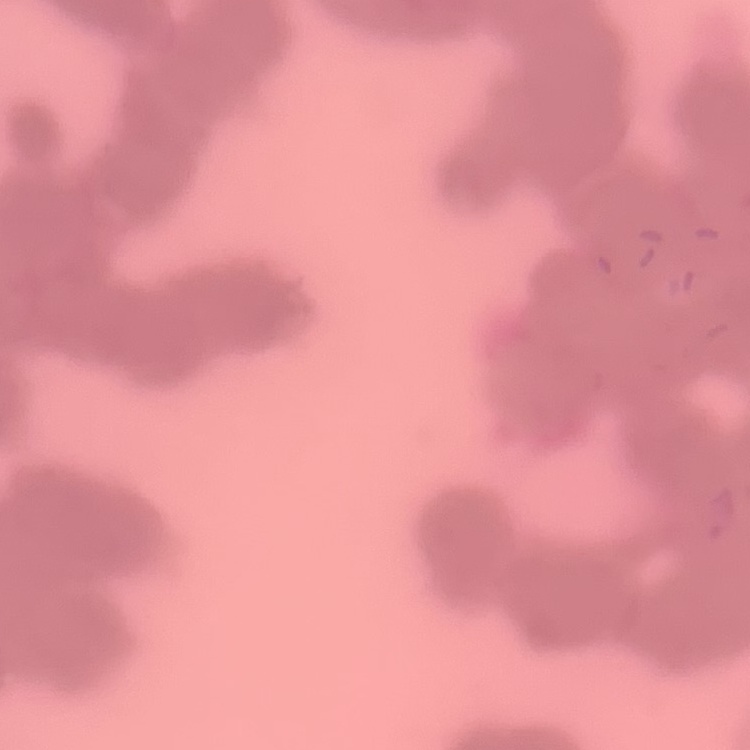

Summary:
  - Red blood cell morphology: rouleaux formation
  - Image type: square crop of a larger photomicrograph
  - Preparation: thin peripheral smear
  - Stain: Field's or Giemsa